Report the malaria status of this cell.
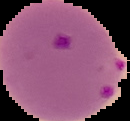
It is parasitized.

Cell region segmented out of the field of view; the surrounding area is masked to black. Image is 130×121 pixels. From a thin blood smear.